Assess the morphology of the red blood cells.
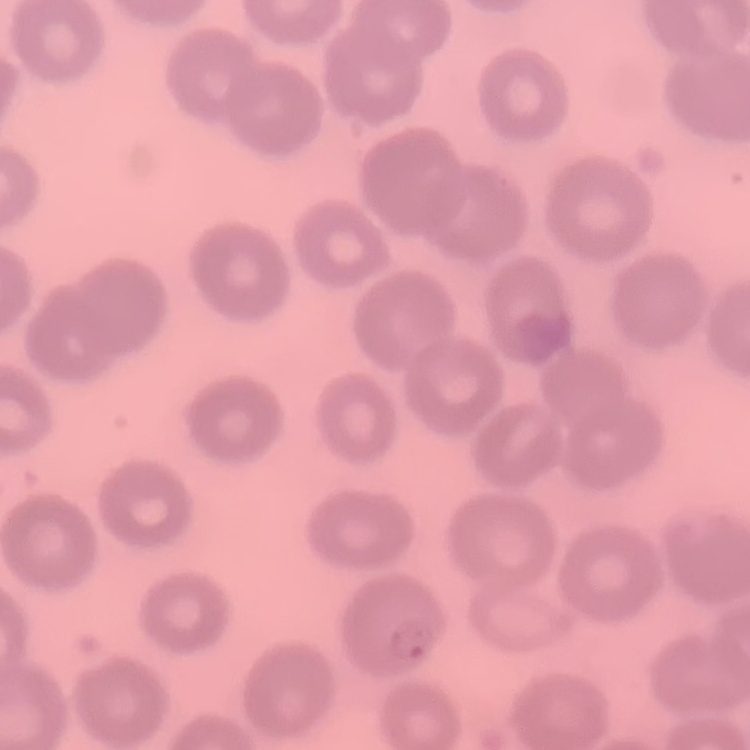
They show no rouleaux formation.

preparation = thin peripheral smear
stain = Field's or Giemsa
image type = square crop of a larger photomicrograph